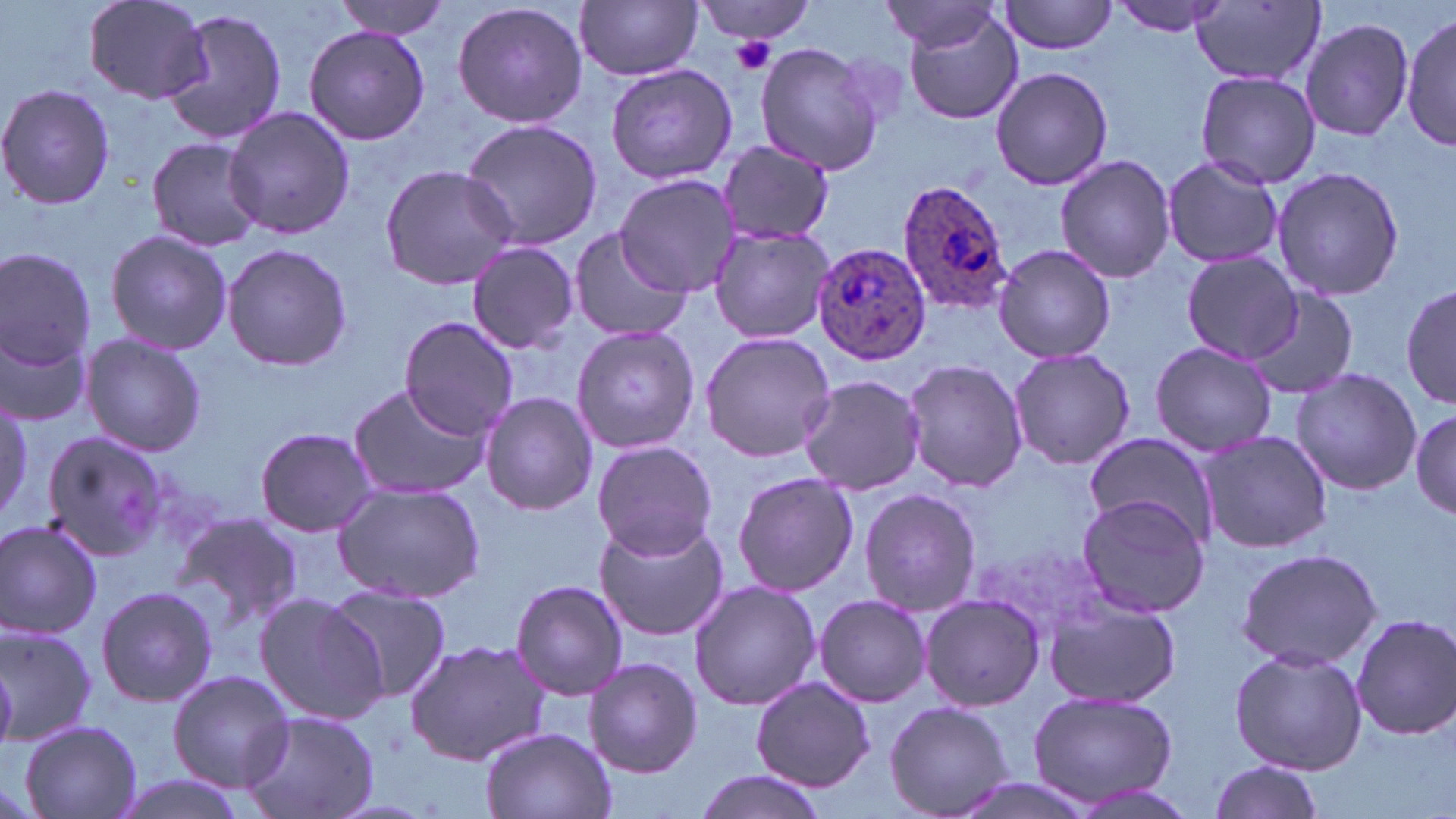

Summary:
  - Coordinate format: approximate bounding boxes as (x1,y1)-(x2,y2) corner pairs in pixels
  - Platelet locations: (729,36)-(776,75)
  - Plasmodium ovale-infected red blood cell locations: (897,180)-(1014,314), (807,244)-(930,367)
  - Uninfected red blood cell locations: (83,0)-(216,105), (328,0)-(453,38), (693,0)-(817,45), (995,0)-(1122,56), (1108,0)-(1235,37), (450,1)-(588,129), (577,1)-(703,81), (877,2)-(1005,54), (1193,3)-(1325,85), (900,7)-(1025,125), (160,11)-(291,144), (1403,11)-(1455,153), (1300,18)-(1415,143), (302,24)-(432,145), (754,41)-(885,176), (604,63)-(739,185), (989,65)-(1113,192), (1192,69)-(1323,188), (0,82)-(117,212), (222,105)-(355,240), (461,119)-(604,252), (147,137)-(265,251), (716,141)-(835,244), (1055,153)-(1176,283), (1160,155)-(1284,270), (378,164)-(520,288), (1271,166)-(1404,303), (612,173)-(741,298), (708,225)-(837,346), (568,227)-(692,342), (104,228)-(233,354), (221,242)-(352,373), (466,242)-(580,353), (990,244)-(1118,362), (0,250)-(97,368), (1181,252)-(1305,362), (1400,283)-(1455,410), (1243,289)-(1355,402), (397,318)-(518,439), (572,324)-(698,455), (1,327)-(94,428), (699,332)-(837,463), (81,333)-(207,457), (1149,341)-(1279,458), (1008,348)-(1135,471), (902,357)-(1028,495), (1290,367)-(1422,498), (798,373)-(924,496), (347,382)-(489,500), (478,390)-(597,516), (0,395)-(31,523), (1410,402)-(1456,522), (253,426)-(378,537), (1193,429)-(1333,555), (40,430)-(169,562), (1084,434)-(1215,541), (592,440)-(718,559), (731,470)-(860,597), (331,482)-(485,604), (858,488)-(983,615), (1076,493)-(1211,618), (171,511)-(303,644), (592,516)-(731,641), (0,519)-(104,640), (1236,546)-(1384,672), (510,579)-(628,700), (689,581)-(819,711), (95,585)-(219,708), (323,585)-(451,704), (919,591)-(1045,714), (252,592)-(386,725), (814,594)-(931,709), (1044,597)-(1181,709), (1350,611)-(1456,740), (0,621)-(98,746), (404,639)-(553,766), (1228,645)-(1367,774), (582,656)-(701,781), (168,670)-(296,791), (750,676)-(876,790), (1026,687)-(1177,807), (885,701)-(1015,819), (240,710)-(379,819), (19,719)-(143,818), (483,727)-(614,819), (1205,759)-(1326,819), (690,769)-(830,819), (107,775)-(252,819), (942,776)-(1108,819)
  - Slide-level diagnosis: Plasmodium ovale
  - Field of view: single
  - Image size: 1456×819 pixels
  - Magnification: 1000x
  - Stain: May-Grünwald-Giemsa
  - Modality: light microscopy
  - Preparation: thin blood smear